State which parasite is depicted.
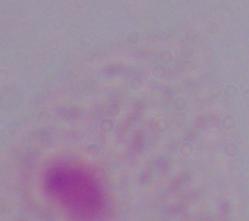
This is a trichomonad.

magnification = 1000x
modality = micrograph